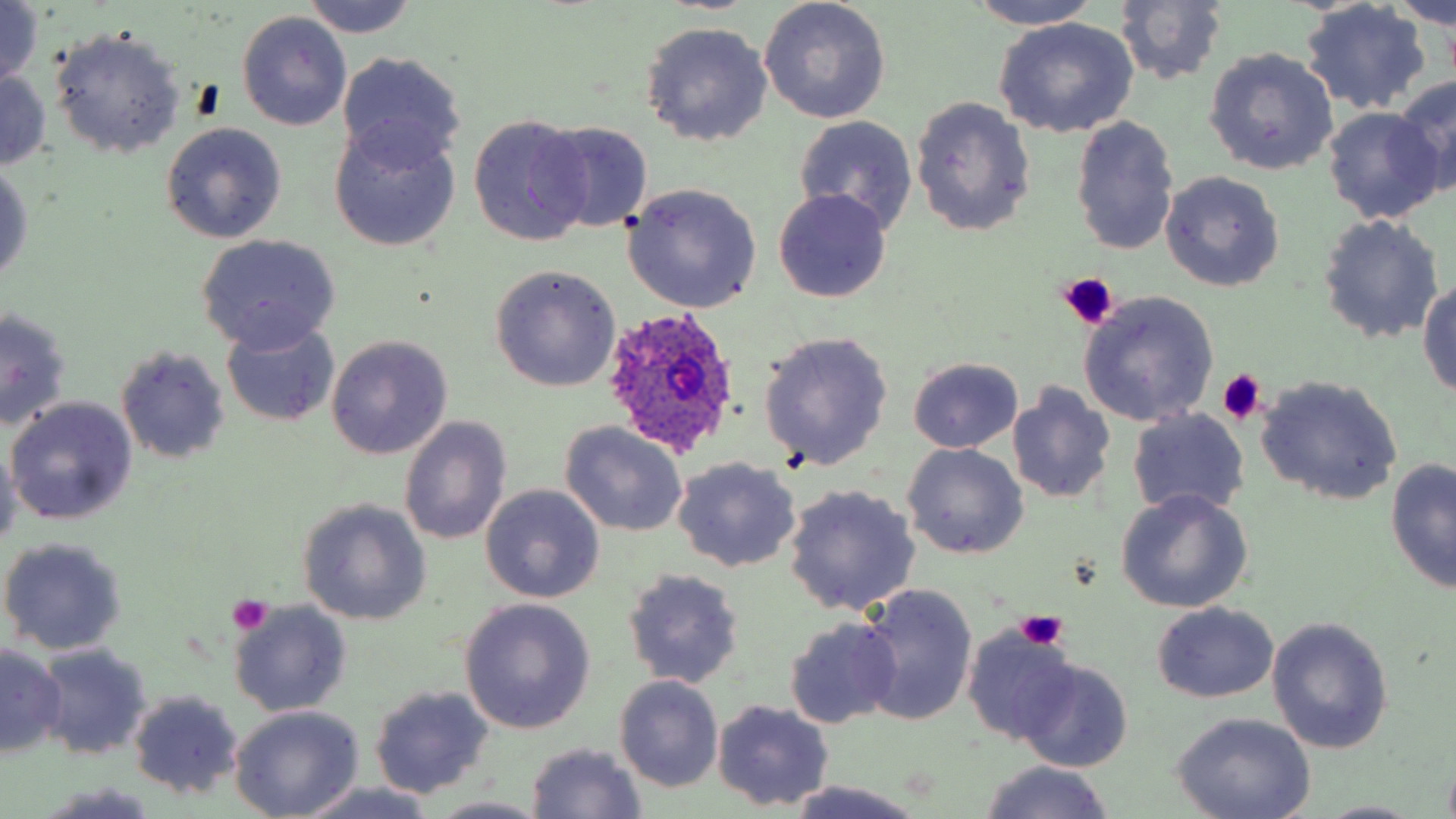 Approximate bounding boxes as (x1,y1)-(x2,y2) corner pairs in pixels. Platelet locations: (1056,273)-(1119,329), (1215,370)-(1267,425), (229,593)-(273,635), (1014,609)-(1069,651). Uninfected red blood cell locations: (300,0)-(420,38), (759,0)-(892,124), (1300,0)-(1432,115), (1393,0)-(1456,29), (966,1)-(1104,31), (1114,1)-(1228,86), (1,2)-(47,90), (239,10)-(351,130), (993,18)-(1139,139), (641,22)-(773,146), (49,26)-(187,159), (1203,48)-(1339,176), (338,50)-(466,172), (0,70)-(49,172), (1395,74)-(1456,196), (910,96)-(1036,236), (1323,108)-(1445,226), (468,114)-(593,247), (794,114)-(919,236), (1070,115)-(1181,258), (329,121)-(460,251), (537,121)-(654,235), (160,122)-(287,244), (0,161)-(33,287), (1160,170)-(1284,292), (622,183)-(763,312), (774,189)-(892,303), (1316,217)-(1444,342), (196,234)-(341,353), (489,265)-(621,392), (1418,278)-(1456,400), (1078,290)-(1219,427), (1,309)-(74,432), (222,321)-(341,425), (759,331)-(894,472), (326,335)-(453,459), (115,345)-(230,465), (907,357)-(1024,452), (1256,375)-(1402,507), (1007,382)-(1116,507), (7,396)-(138,524), (1128,409)-(1251,519), (399,416)-(512,545), (562,421)-(689,536), (0,440)-(21,554), (903,443)-(1028,560), (671,457)-(802,573), (1385,458)-(1455,594), (480,484)-(605,603), (783,484)-(921,616), (1114,490)-(1253,614), (298,499)-(432,625), (0,537)-(128,655), (623,568)-(745,689), (857,584)-(978,728), (460,599)-(594,733), (227,600)-(352,718), (1153,602)-(1275,702), (1268,616)-(1393,754), (784,618)-(902,728), (962,626)-(1076,746), (36,642)-(153,760), (0,645)-(68,756), (1017,659)-(1132,773), (614,675)-(724,793), (369,684)-(495,799), (127,689)-(246,800), (713,699)-(834,809), (231,706)-(363,818), (1171,712)-(1319,819), (526,743)-(647,818), (974,760)-(1118,818), (783,781)-(928,819), (294,782)-(442,819), (40,786)-(165,819), (426,797)-(552,819), (1314,799)-(1427,817). Plasmodium ovale-infected red blood cell locations: (602,304)-(742,458). Slide-level diagnosis: Plasmodium ovale. Thin blood film. Image is 1456×819 pixels. May-Grünwald-Giemsa-stained preparation. Captured at 1000x magnification. One field of a larger specimen. Optical microscopy.